Assess the morphology of the red blood cells.
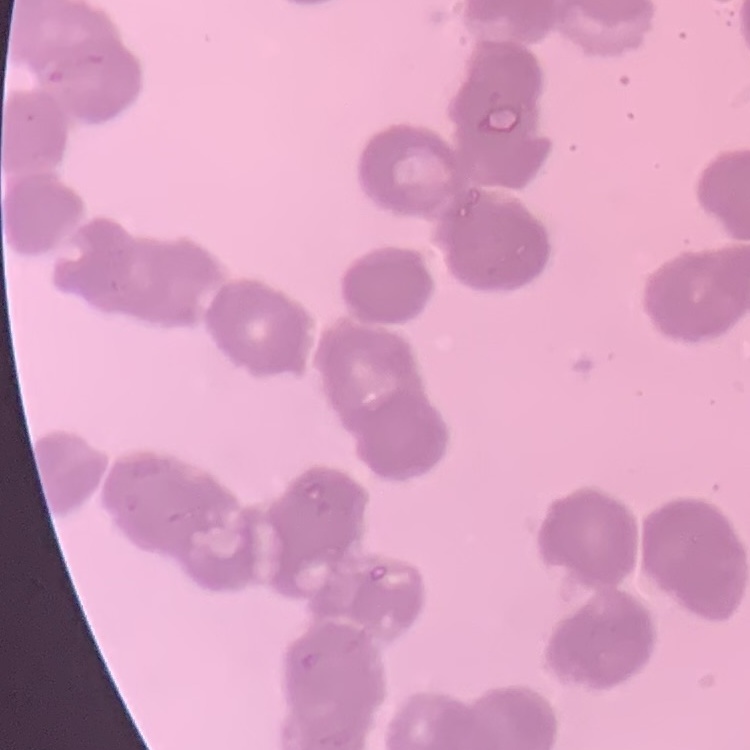
Rouleaux formation.

preparation = thin blood film
image type = one tile cut from a larger photomicrograph
stain = Field's or Giemsa